Outline platelets.
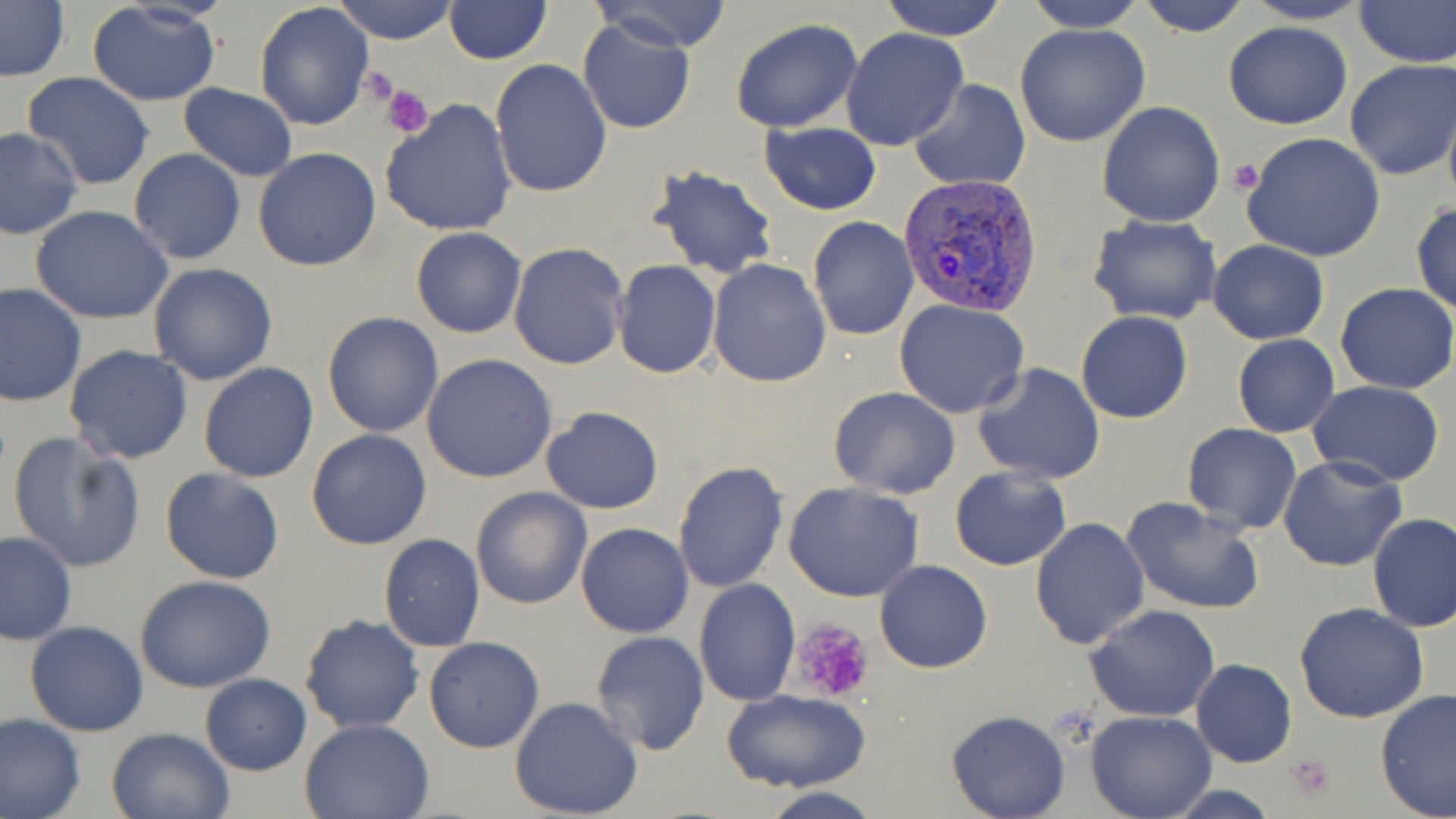
Approximate bounding boxes as named x1/y1/x2/y2 corners in pixels.
Platelets: (x1=359, y1=68, x2=400, y2=112), (x1=383, y1=87, x2=433, y2=138), (x1=1229, y1=159, x2=1265, y2=195), (x1=792, y1=620, x2=874, y2=704), (x1=1287, y1=754, x2=1339, y2=801).

Uninfected red blood cell locations: (x1=332, y1=0, x2=459, y2=45), (x1=592, y1=0, x2=734, y2=53), (x1=877, y1=0, x2=1009, y2=40), (x1=1021, y1=0, x2=1150, y2=32), (x1=1135, y1=0, x2=1252, y2=36), (x1=1242, y1=0, x2=1371, y2=24), (x1=1352, y1=0, x2=1454, y2=67), (x1=1, y1=1, x2=70, y2=82), (x1=443, y1=1, x2=551, y2=65), (x1=85, y1=3, x2=222, y2=106), (x1=254, y1=4, x2=376, y2=132), (x1=577, y1=17, x2=698, y2=135), (x1=729, y1=19, x2=862, y2=134), (x1=1223, y1=20, x2=1352, y2=130), (x1=1013, y1=24, x2=1152, y2=148), (x1=841, y1=29, x2=968, y2=152), (x1=490, y1=58, x2=613, y2=197), (x1=1345, y1=59, x2=1456, y2=182), (x1=23, y1=72, x2=155, y2=191), (x1=909, y1=79, x2=1031, y2=191), (x1=177, y1=83, x2=298, y2=181), (x1=1441, y1=91, x2=1456, y2=211), (x1=380, y1=99, x2=518, y2=236), (x1=1096, y1=101, x2=1226, y2=227), (x1=758, y1=121, x2=882, y2=216), (x1=0, y1=127, x2=81, y2=240), (x1=1240, y1=130, x2=1387, y2=263), (x1=129, y1=148, x2=246, y2=266), (x1=254, y1=148, x2=382, y2=272), (x1=646, y1=162, x2=780, y2=280), (x1=1411, y1=201, x2=1456, y2=317), (x1=29, y1=205, x2=174, y2=324), (x1=1085, y1=215, x2=1224, y2=326), (x1=808, y1=216, x2=919, y2=340), (x1=410, y1=227, x2=527, y2=338), (x1=1207, y1=239, x2=1328, y2=345), (x1=508, y1=241, x2=630, y2=370), (x1=611, y1=260, x2=721, y2=379), (x1=708, y1=260, x2=829, y2=387), (x1=148, y1=263, x2=278, y2=385), (x1=0, y1=283, x2=87, y2=406), (x1=1334, y1=283, x2=1456, y2=396), (x1=894, y1=300, x2=1030, y2=420), (x1=322, y1=311, x2=443, y2=437), (x1=1075, y1=311, x2=1193, y2=424), (x1=1232, y1=335, x2=1340, y2=438), (x1=65, y1=345, x2=194, y2=464), (x1=422, y1=354, x2=558, y2=483), (x1=199, y1=362, x2=318, y2=483), (x1=974, y1=362, x2=1106, y2=485), (x1=1306, y1=381, x2=1445, y2=487), (x1=828, y1=386, x2=961, y2=499), (x1=540, y1=406, x2=664, y2=514), (x1=1181, y1=422, x2=1303, y2=535), (x1=305, y1=428, x2=434, y2=550), (x1=8, y1=433, x2=146, y2=574), (x1=1227, y1=436, x2=1368, y2=557), (x1=1277, y1=455, x2=1407, y2=573), (x1=674, y1=460, x2=789, y2=594), (x1=949, y1=466, x2=1071, y2=570), (x1=159, y1=467, x2=286, y2=585), (x1=784, y1=482, x2=925, y2=604), (x1=471, y1=486, x2=593, y2=610), (x1=1120, y1=495, x2=1265, y2=616), (x1=1367, y1=512, x2=1456, y2=633), (x1=1028, y1=517, x2=1150, y2=652), (x1=576, y1=523, x2=693, y2=638), (x1=0, y1=531, x2=76, y2=645), (x1=377, y1=534, x2=486, y2=653), (x1=874, y1=560, x2=993, y2=674), (x1=135, y1=574, x2=277, y2=692), (x1=694, y1=578, x2=800, y2=707), (x1=1294, y1=602, x2=1429, y2=723), (x1=1084, y1=604, x2=1220, y2=723), (x1=299, y1=614, x2=425, y2=735), (x1=25, y1=622, x2=148, y2=735), (x1=589, y1=631, x2=710, y2=757), (x1=423, y1=637, x2=545, y2=753), (x1=1191, y1=659, x2=1296, y2=768), (x1=200, y1=674, x2=312, y2=774), (x1=1374, y1=687, x2=1456, y2=819), (x1=719, y1=688, x2=872, y2=795), (x1=508, y1=696, x2=643, y2=818), (x1=945, y1=710, x2=1071, y2=819), (x1=1085, y1=710, x2=1216, y2=819), (x1=0, y1=712, x2=84, y2=819), (x1=299, y1=718, x2=435, y2=819), (x1=106, y1=726, x2=233, y2=819), (x1=1160, y1=782, x2=1281, y2=818), (x1=753, y1=786, x2=884, y2=819). Plasmodium vivax-infected red blood cell locations: (x1=897, y1=173, x2=1041, y2=318). Slide-level diagnosis: Plasmodium vivax. May-Grünwald-Giemsa-stained preparation. One field of a larger specimen. Thin blood smear. 1000x magnification. Image is 1456×819 pixels. Optical microscopy.